Identify the parasite.
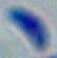

This is Toxoplasma gondii.

1000x magnification. Photomicrograph.